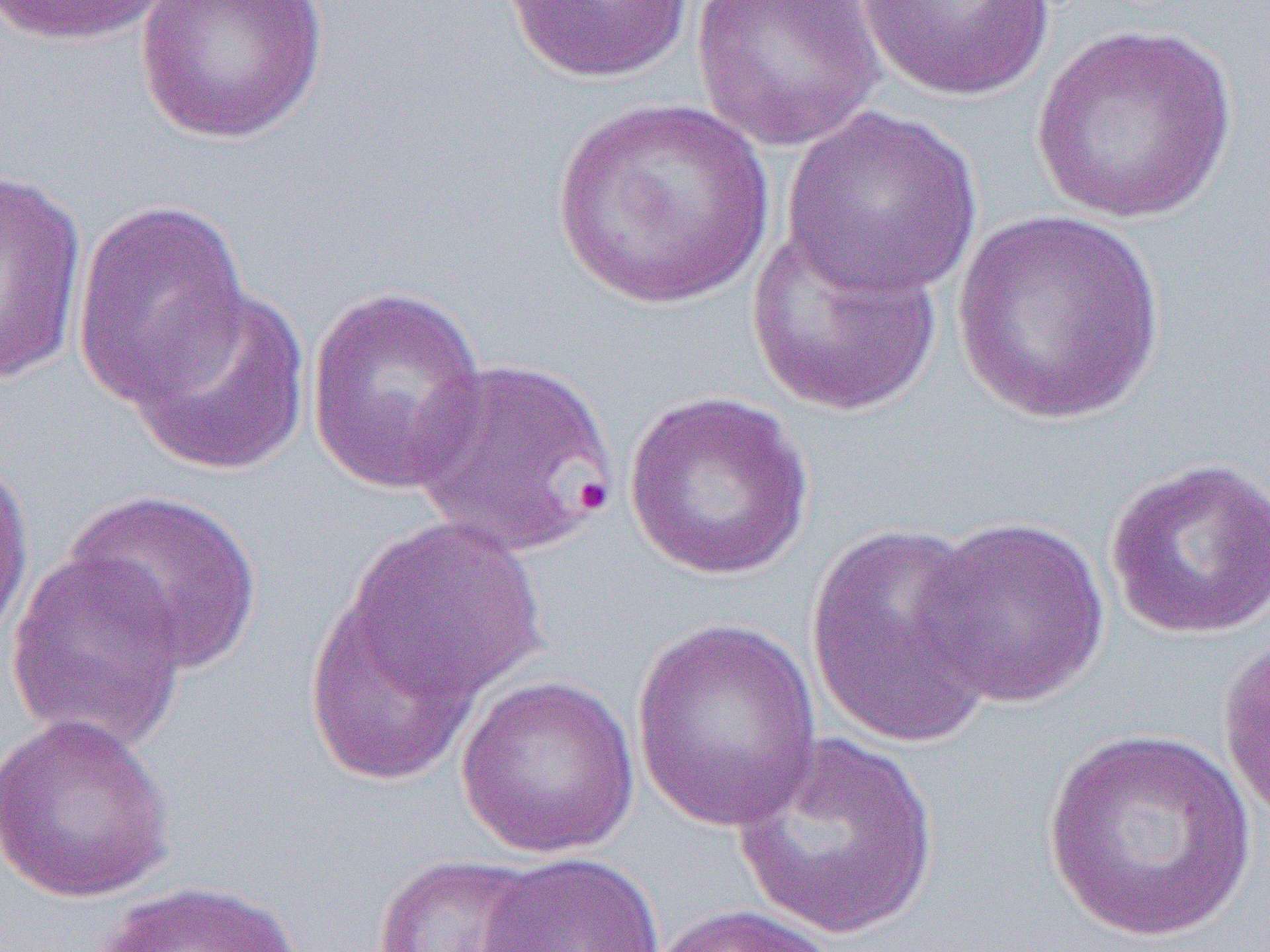 Approximate bounding boxes as [x1, y1, x2, y2] in pixels. Uninfected red blood cell locations: [2, 0, 177, 47], [136, 0, 328, 144], [691, 0, 885, 152], [856, 0, 1057, 103], [500, 1, 694, 84], [1030, 22, 1239, 226], [551, 99, 774, 310], [782, 105, 984, 300], [0, 167, 88, 384], [71, 198, 251, 406], [948, 209, 1169, 426], [744, 222, 945, 418], [125, 285, 314, 477], [304, 285, 490, 496], [411, 356, 617, 557], [622, 389, 816, 580], [0, 450, 36, 652], [1103, 457, 1270, 640], [61, 488, 264, 676], [914, 515, 1111, 708], [346, 518, 548, 705], [805, 523, 999, 750], [4, 546, 191, 755], [304, 590, 482, 787], [630, 619, 823, 831], [1218, 628, 1270, 827], [455, 675, 641, 859], [0, 711, 176, 904], [1039, 728, 1260, 945], [728, 731, 940, 943], [478, 851, 666, 952], [373, 854, 550, 952], [89, 880, 308, 952], [646, 904, 842, 952]. Slide-level diagnosis: Plasmodium falciparum. Thin blood film. Single field of view. 1000x magnification. Light microscopy. Image is 1270×952 pixels.